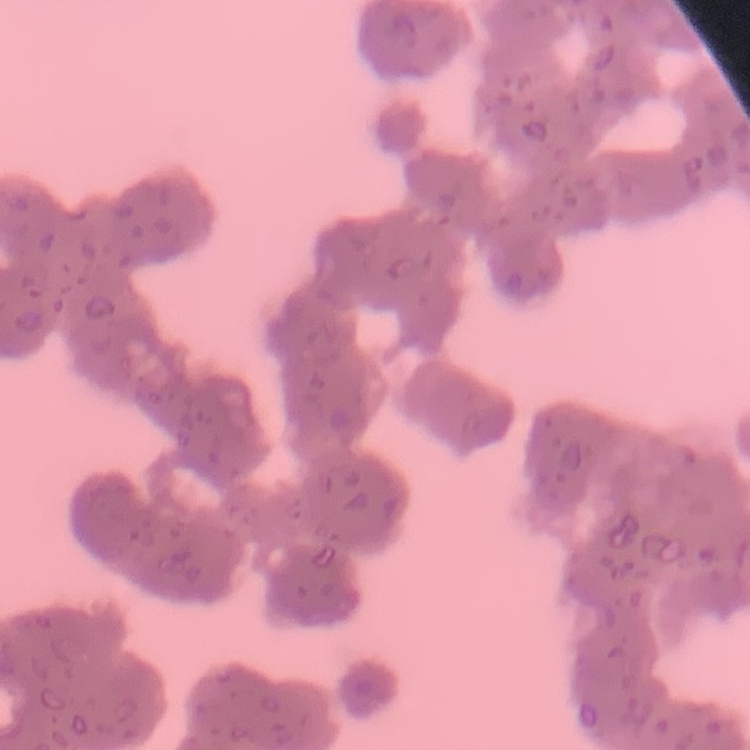
Summary:
  - Red blood cell morphology: rouleaux formation
  - Preparation: thin blood film
  - Stain: Field's or Giemsa
  - Image type: one tile cut from a larger photomicrograph